Report the malaria status of this cell.
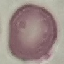

Uninfected.

stain = Giemsa
preparation = thin blood smear
image type = automatically extracted cell patch, resized to 64 × 64 pixels
capture = smartphone through the microscope eyepiece